State which parasite is depicted.
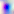
Toxoplasma gondii.

{
  "modality": "photomicrograph",
  "magnification": "400x"
}